Report the malaria status of this cell.
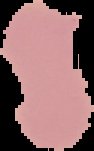
Uninfected.

Segmented cell region on a black background. Image is 94×151 pixels. From a thin blood smear.